State which parasite is depicted.
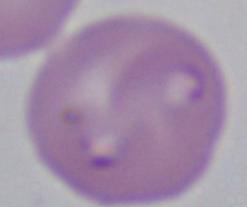

Babesia.

Summary:
  - Modality: photomicrograph
  - Magnification: 1000x